Locate and identify every blood parasite.
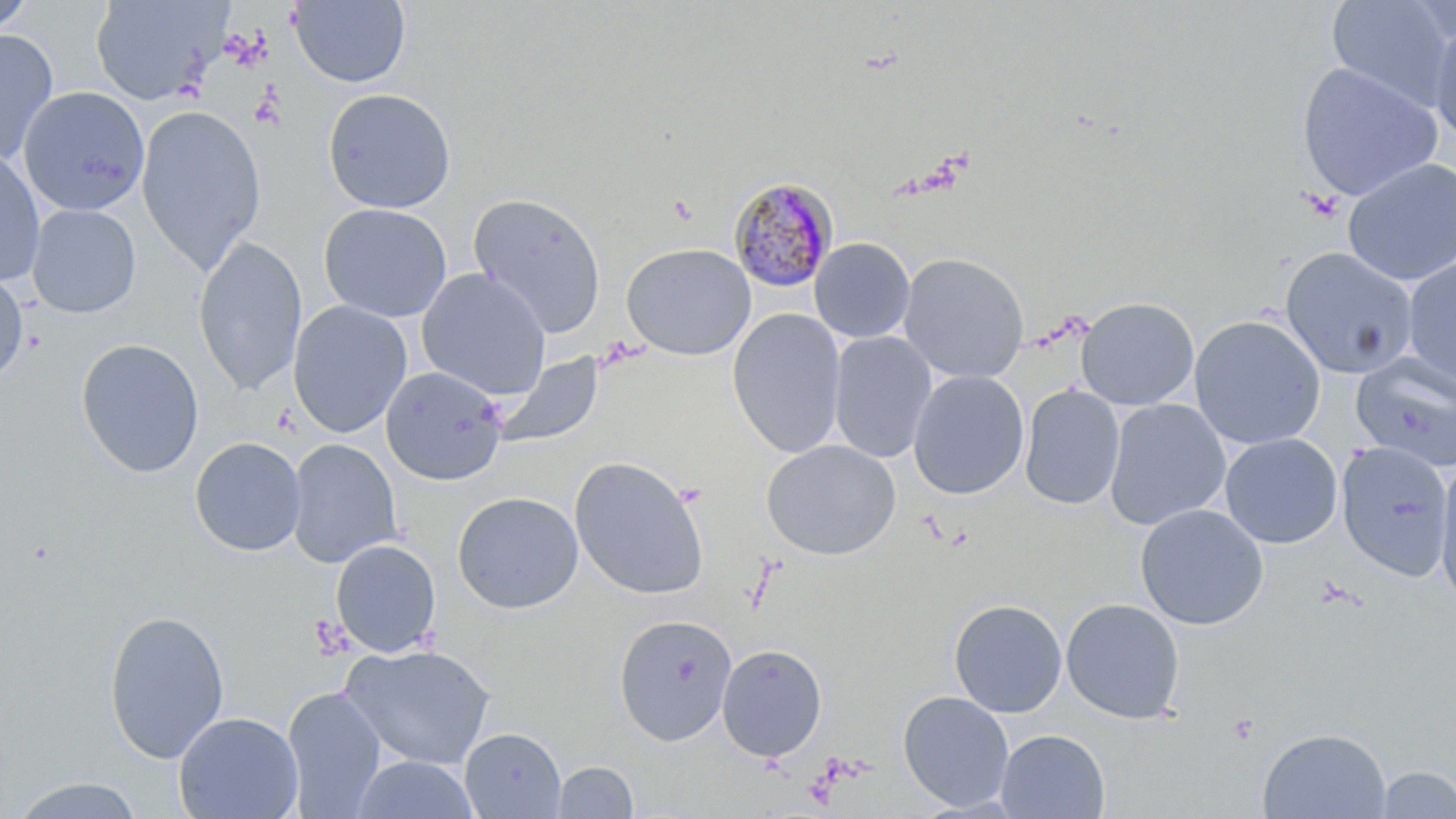
Approximate bounding boxes as (x1, y1, x2, y2) in pixels.
Plasmodium malariae-infected red blood cells: (729, 176, 841, 293).
No Plasmodium falciparum, Plasmodium ovale, Plasmodium vivax, Babesia divergens, or Trypanosoma brucei observed.

Summary:
  - Uninfected red blood cell locations: (0, 0, 38, 37), (89, 0, 230, 106), (1325, 0, 1454, 109), (289, 1, 410, 87), (1428, 18, 1456, 147), (0, 29, 59, 165), (1296, 62, 1443, 202), (18, 86, 150, 216), (323, 88, 456, 213), (135, 105, 267, 275), (0, 147, 45, 286), (1342, 158, 1456, 285), (467, 192, 607, 338), (318, 203, 452, 322), (26, 204, 141, 319), (192, 235, 308, 395), (810, 238, 915, 343), (621, 242, 756, 360), (1280, 248, 1418, 379), (898, 252, 1030, 383), (1402, 255, 1456, 389), (0, 266, 29, 384), (416, 268, 551, 400), (1076, 296, 1199, 411), (287, 300, 413, 438), (726, 308, 846, 458), (1189, 314, 1326, 450), (828, 331, 938, 463), (75, 338, 204, 478), (494, 353, 604, 448), (1351, 354, 1456, 473), (380, 366, 508, 486), (907, 370, 1029, 500), (1019, 385, 1125, 511), (1104, 398, 1231, 530), (1220, 433, 1342, 548), (189, 436, 306, 557), (285, 438, 402, 568), (761, 439, 902, 561), (1336, 442, 1453, 581), (569, 455, 710, 601), (1435, 456, 1456, 609), (451, 491, 584, 614), (1134, 504, 1269, 630), (330, 538, 441, 658), (1060, 598, 1185, 724), (949, 599, 1067, 717), (103, 609, 230, 764), (613, 614, 737, 745), (340, 643, 497, 770), (716, 644, 827, 762), (281, 686, 387, 818), (898, 690, 1014, 812), (173, 711, 303, 819), (1257, 727, 1392, 819), (459, 728, 567, 818), (995, 729, 1110, 818), (348, 755, 481, 819), (551, 760, 638, 818), (1373, 765, 1456, 818), (8, 776, 147, 818)
  - Platelet locations: (1228, 714, 1258, 745)
  - Slide-level diagnosis: Plasmodium malariae
  - Modality: light microscopy
  - Image size: 1456×819 pixels
  - Magnification: 1000x
  - Stain: May-Grünwald-Giemsa
  - Field of view: single
  - Preparation: thin blood film